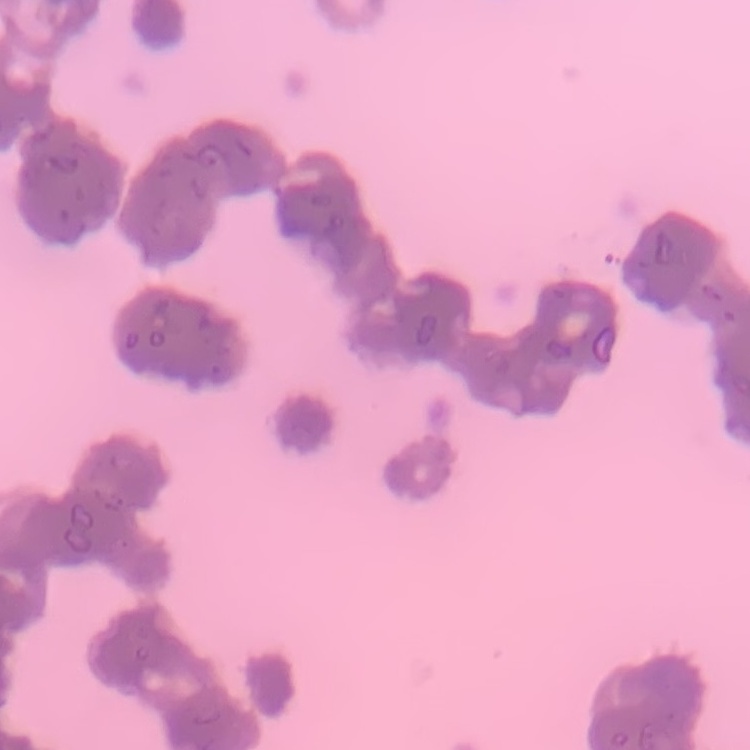
The red blood cells show rouleaux formation. Field's or Giemsa stain. Thin blood smear. One tile cut from a larger photomicrograph.